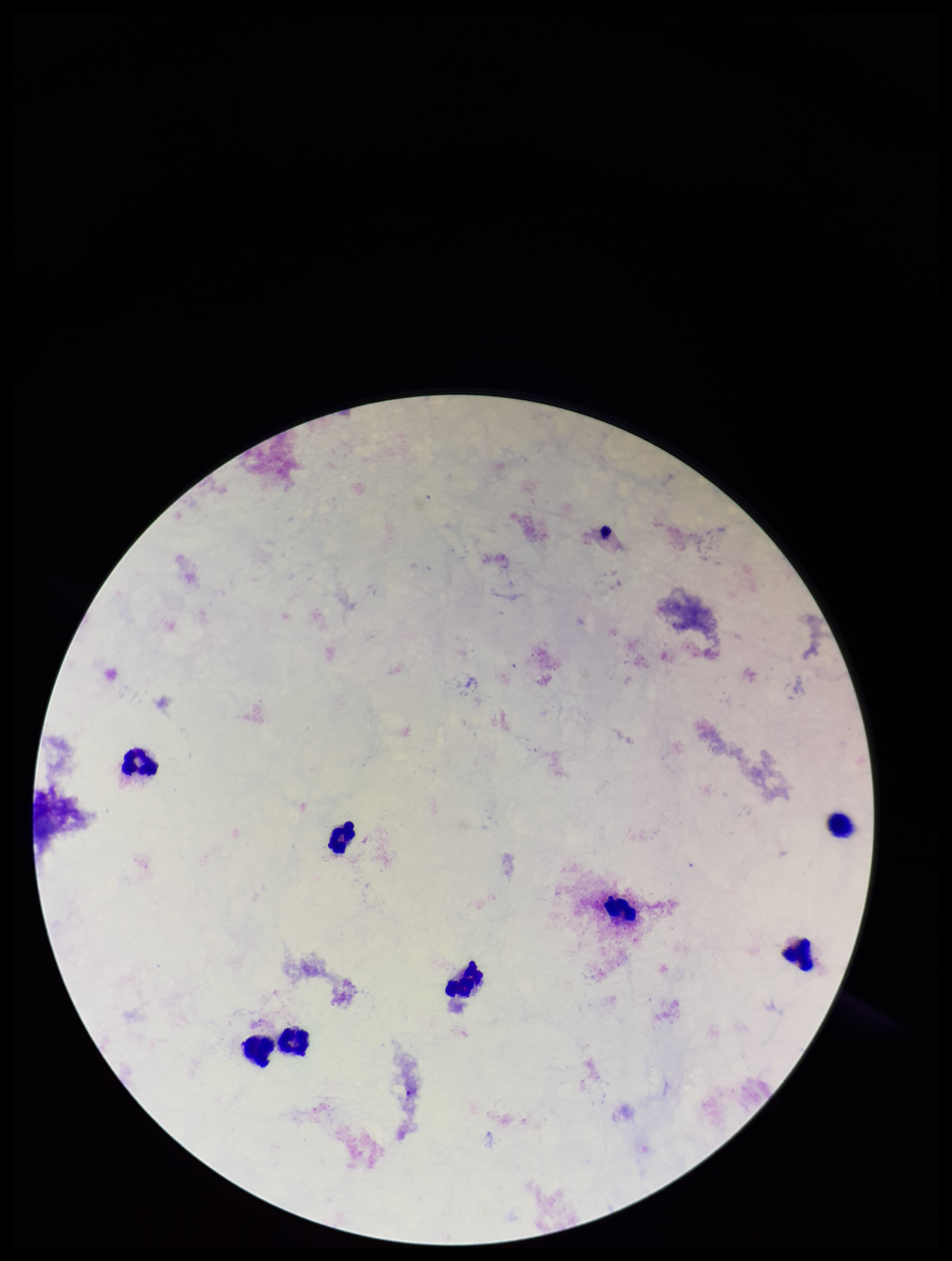

Summary:
  - Patient malaria status: negative
  - Leukocyte count: 8
  - Stain: Giemsa
  - Capture: smartphone photograph through the microscope eyepiece
  - Preparation: thick smear
  - Field of view: single
  - Parasite count: 0
  - Plasmodium parasites: none identified
  - Image size: 952×1261 pixels